Give the extent of all Plasmodium falciparum-infected red blood cells.
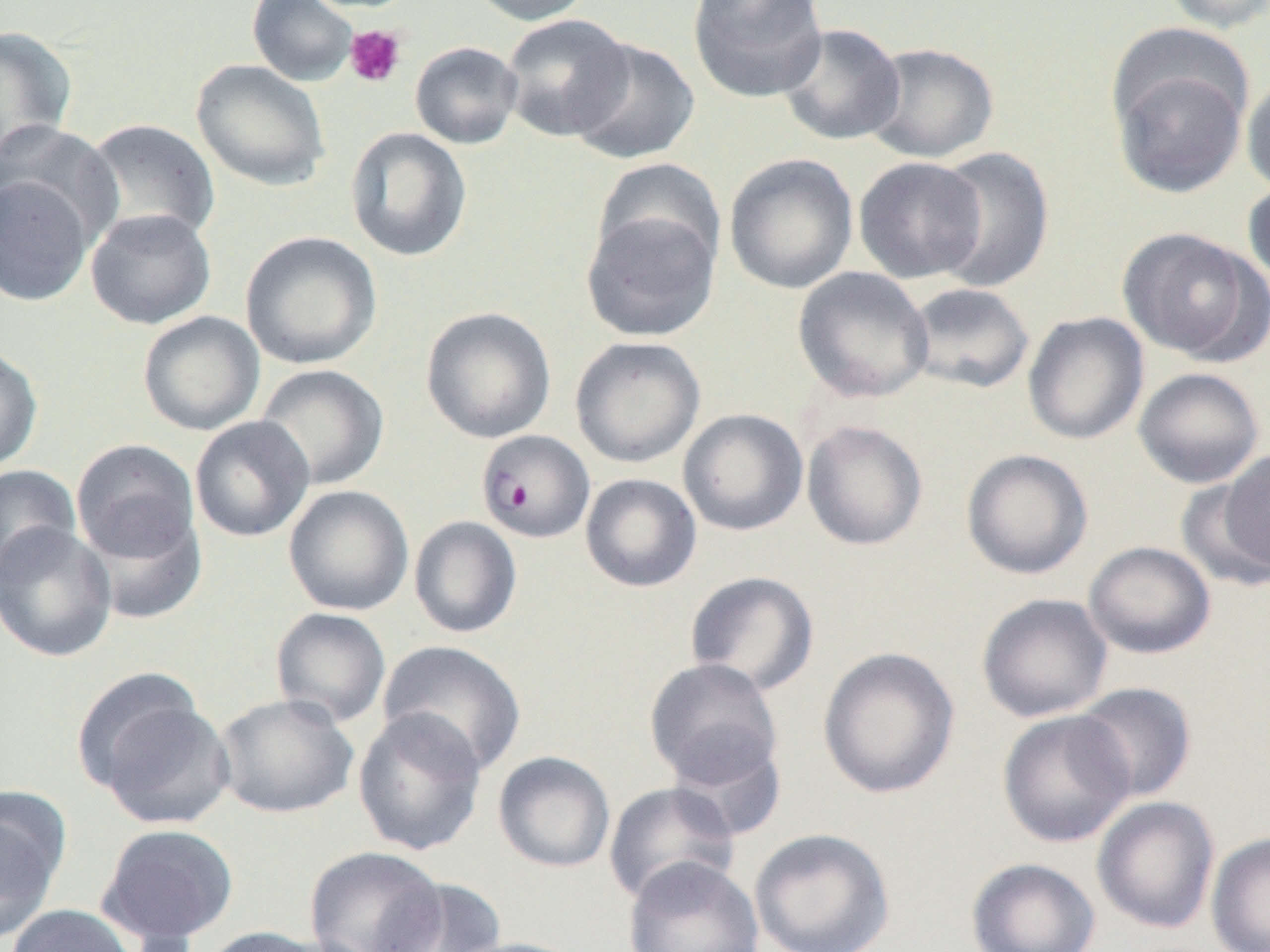

Approximate bounding boxes as named x1/y1/x2/y2 corners in pixels.
Plasmodium falciparum-infected red blood cells: (x1=476, y1=429, x2=596, y2=543).

slide_level_diagnosis: Plasmodium falciparum
preparation: thin blood smear
image_size: 1270×952 pixels
modality: optical microscopy
uninfected_red_blood_cell_locations: 'approximate bounding boxes as named x1/y1/x2/y2 corners in pixels: (x1=247, y1=0, x2=359, y2=87), (x1=465, y1=0, x2=596, y2=26), (x1=687, y1=0, x2=828, y2=103), (x1=1159, y1=0, x2=1270, y2=33), (x1=500, y1=13, x2=634, y2=142), (x1=777, y1=22, x2=906, y2=146), (x1=0, y1=26, x2=78, y2=165), (x1=568, y1=38, x2=699, y2=165), (x1=410, y1=41, x2=523, y2=149), (x1=863, y1=42, x2=999, y2=163), (x1=1109, y1=53, x2=1251, y2=199), (x1=191, y1=58, x2=331, y2=192), (x1=1241, y1=72, x2=1270, y2=198), (x1=82, y1=118, x2=220, y2=246), (x1=0, y1=120, x2=123, y2=250), (x1=345, y1=126, x2=473, y2=262), (x1=930, y1=145, x2=1055, y2=293), (x1=723, y1=153, x2=859, y2=295), (x1=591, y1=156, x2=727, y2=274), (x1=853, y1=156, x2=988, y2=284), (x1=0, y1=175, x2=94, y2=307), (x1=1242, y1=179, x2=1270, y2=290), (x1=85, y1=208, x2=217, y2=330), (x1=581, y1=208, x2=720, y2=342), (x1=1117, y1=227, x2=1267, y2=363), (x1=240, y1=231, x2=382, y2=369), (x1=793, y1=266, x2=934, y2=403), (x1=903, y1=282, x2=1035, y2=395), (x1=420, y1=307, x2=556, y2=444), (x1=137, y1=311, x2=265, y2=436), (x1=1022, y1=311, x2=1150, y2=445), (x1=569, y1=336, x2=706, y2=468), (x1=0, y1=345, x2=44, y2=474), (x1=255, y1=364, x2=389, y2=491), (x1=1133, y1=367, x2=1265, y2=488), (x1=678, y1=408, x2=808, y2=536), (x1=189, y1=416, x2=315, y2=542), (x1=801, y1=420, x2=928, y2=551), (x1=70, y1=438, x2=200, y2=564), (x1=1216, y1=447, x2=1269, y2=577), (x1=960, y1=448, x2=1093, y2=579), (x1=0, y1=464, x2=81, y2=581), (x1=580, y1=473, x2=702, y2=592), (x1=1176, y1=476, x2=1269, y2=592), (x1=283, y1=484, x2=414, y2=616), (x1=79, y1=507, x2=207, y2=625), (x1=408, y1=515, x2=522, y2=638), (x1=0, y1=522, x2=118, y2=661), (x1=1082, y1=541, x2=1216, y2=659), (x1=684, y1=570, x2=819, y2=696), (x1=976, y1=592, x2=1113, y2=722), (x1=270, y1=607, x2=392, y2=728), (x1=377, y1=640, x2=527, y2=775), (x1=818, y1=646, x2=960, y2=799), (x1=644, y1=657, x2=784, y2=790), (x1=81, y1=682, x2=237, y2=829), (x1=1072, y1=682, x2=1197, y2=803), (x1=214, y1=693, x2=359, y2=819), (x1=351, y1=708, x2=488, y2=857), (x1=997, y1=709, x2=1135, y2=848), (x1=665, y1=734, x2=788, y2=841), (x1=493, y1=751, x2=616, y2=873), (x1=603, y1=781, x2=740, y2=905), (x1=0, y1=791, x2=69, y2=941), (x1=1091, y1=795, x2=1220, y2=934), (x1=96, y1=822, x2=239, y2=946), (x1=748, y1=827, x2=895, y2=952), (x1=1206, y1=831, x2=1270, y2=952), (x1=303, y1=846, x2=447, y2=952), (x1=624, y1=857, x2=764, y2=952), (x1=965, y1=857, x2=1101, y2=952), (x1=373, y1=879, x2=507, y2=952), (x1=5, y1=904, x2=139, y2=952), (x1=198, y1=926, x2=337, y2=951), (x1=446, y1=937, x2=588, y2=952)'
magnification: 1000x
platelet_locations: 'approximate bounding boxes as named x1/y1/x2/y2 corners in pixels: (x1=344, y1=25, x2=407, y2=88)'
field_of_view: single